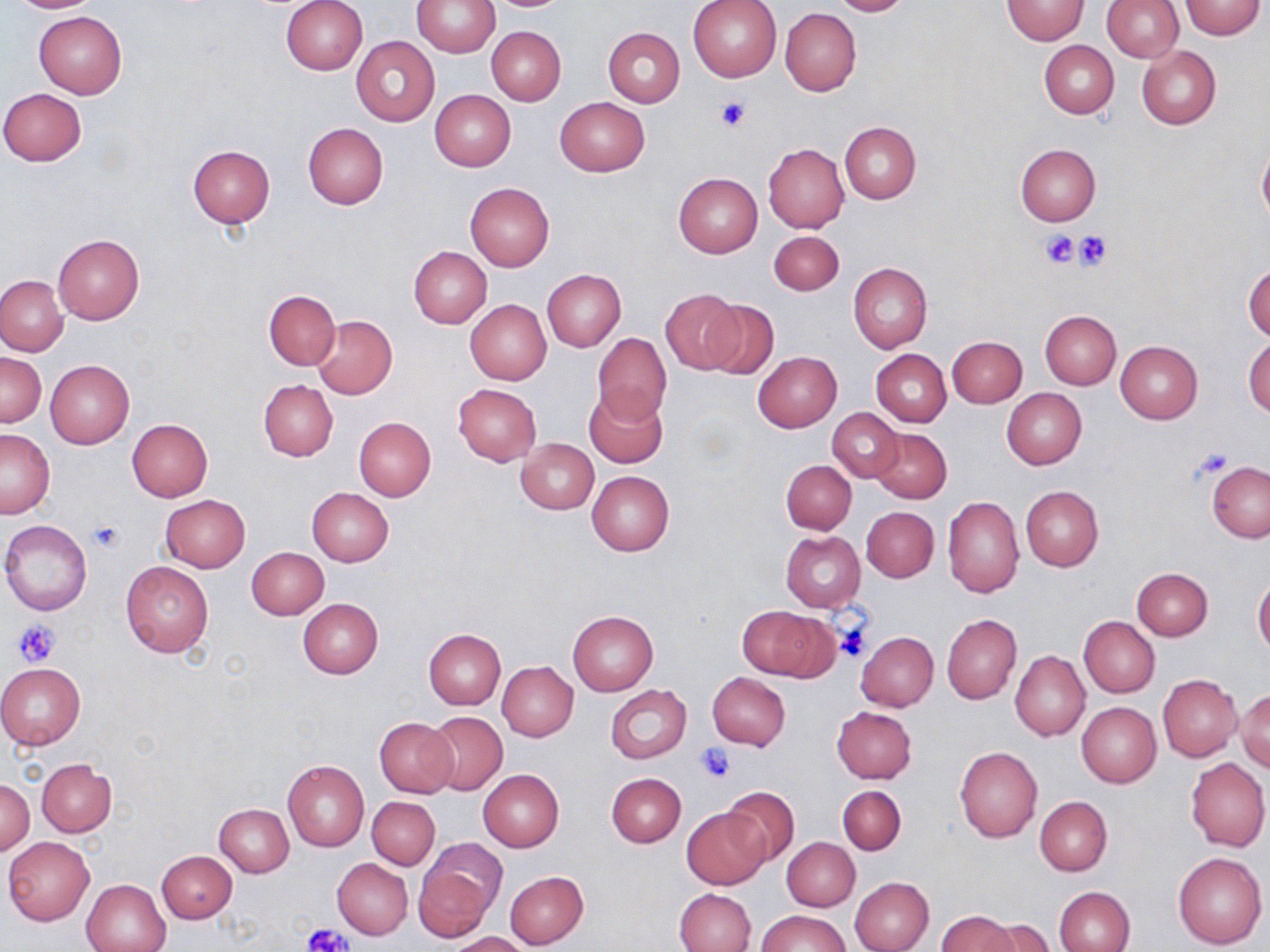
slide-level diagnosis = negative for blood parasites
stain = May-Grünwald-Giemsa
field of view = single
preparation = thin blood film
modality = light microscopy
image size = 1270×952 pixels
uninfected red blood cell locations = approximate bounding boxes as (x1,y1)-(x2,y2) corner pairs in pixels: (5,0)-(104,13), (281,0)-(367,75), (414,0)-(499,56), (687,0)-(781,81), (829,0)-(910,16), (1002,0)-(1088,44), (1102,0)-(1182,61), (1181,0)-(1265,40), (780,8)-(861,95), (33,11)-(127,98), (486,26)-(566,104), (603,27)-(685,106), (351,36)-(439,125), (1039,40)-(1119,119), (1137,46)-(1221,129), (0,88)-(87,166), (430,90)-(516,170), (554,97)-(649,177), (839,121)-(920,205), (302,122)-(388,208), (766,134)-(921,218), (1257,142)-(1270,229), (1015,143)-(1101,226), (763,144)-(848,232), (187,145)-(275,227), (673,173)-(762,258), (465,182)-(554,272), (768,230)-(844,296), (53,235)-(144,324), (408,246)-(491,327), (1244,261)-(1270,343), (848,263)-(932,352), (542,269)-(625,352), (0,276)-(68,355), (264,289)-(340,369), (662,289)-(744,373), (701,298)-(779,381), (465,300)-(552,385), (1041,310)-(1121,389), (311,314)-(398,400), (592,333)-(672,426), (1244,335)-(1270,418), (947,336)-(1027,408), (1115,340)-(1203,423), (870,348)-(951,427), (753,351)-(841,432), (1,352)-(45,427), (45,360)-(134,447), (257,379)-(338,461), (453,384)-(541,466), (583,386)-(666,469), (1002,388)-(1086,469), (827,408)-(903,481), (354,417)-(436,500), (127,418)-(213,501), (868,427)-(951,503), (0,428)-(54,518), (516,438)-(599,514), (782,460)-(856,535), (1208,462)-(1269,542), (587,471)-(675,556), (1020,486)-(1103,571), (307,488)-(394,567), (159,495)-(250,573), (942,495)-(1023,597), (862,506)-(938,582), (1,520)-(93,614), (780,531)-(865,612), (247,547)-(328,619), (120,560)-(214,657), (1132,568)-(1212,641), (1253,576)-(1270,659), (297,598)-(383,678), (737,604)-(835,681), (567,611)-(659,696), (941,614)-(1021,705), (1079,616)-(1159,698), (423,629)-(505,708), (856,631)-(938,712), (1011,651)-(1090,740), (1,662)-(85,751), (497,662)-(577,742), (708,672)-(791,751), (1158,674)-(1243,762), (604,685)-(692,765), (1235,689)-(1270,772), (1076,702)-(1161,788), (831,706)-(917,783), (422,711)-(507,796), (374,717)-(458,798), (954,746)-(1042,841), (1186,757)-(1269,851), (37,759)-(115,836), (283,760)-(369,852), (478,769)-(565,852), (607,772)-(686,848), (1,780)-(34,854), (837,785)-(906,855), (720,786)-(800,866), (367,796)-(440,870), (1035,796)-(1113,876), (214,803)-(293,877), (682,809)-(767,889), (3,836)-(95,925), (782,839)-(860,911), (416,840)-(505,939), (157,850)-(236,922), (1172,851)-(1266,949), (332,858)-(413,939), (504,870)-(588,948), (850,877)-(933,952), (82,878)-(171,952), (1055,886)-(1136,952), (676,888)-(756,952), (757,911)-(851,952), (937,911)-(1019,952), (976,917)-(1056,952), (450,931)-(533,952)
platelet locations = approximate bounding boxes as (x1,y1)-(x2,y2) corner pairs in pixels: (715,97)-(750,131), (1074,229)-(1111,270), (1040,230)-(1080,268), (89,520)-(124,552), (12,619)-(60,669), (833,621)-(872,661), (695,743)-(736,782), (303,924)-(351,950)
magnification = 1000x